Assess this cell for malaria.
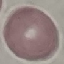

It is uninfected.

Summary:
  - Stain: Giemsa
  - Image type: automatically extracted cell patch, resized to 64 × 64 pixels
  - Capture: smartphone through the microscope eyepiece
  - Preparation: thin blood film